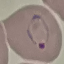

Summary:
  - Malaria status: parasitized
  - Image type: automatically extracted cell patch, resized to 64 × 64 pixels
  - Preparation: thin blood smear
  - Stain: Giemsa
  - Capture: smartphone through the microscope eyepiece